State the blood parasite species.
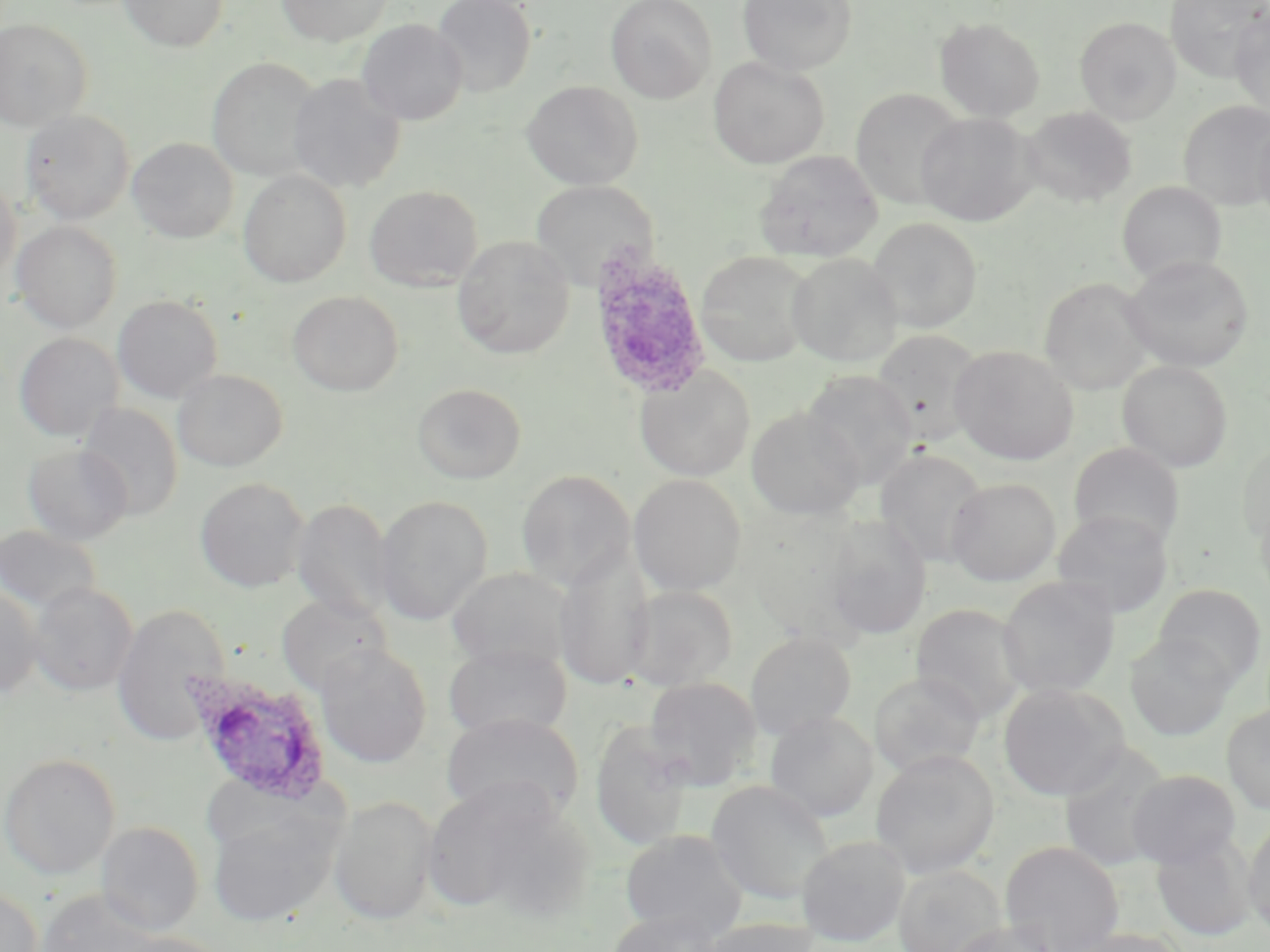
Plasmodium ovale.

Approximate bounding boxes as [x1, y1, x2, y2] in pixels. Plasmodium ovale-infected red blood cell locations: [586, 247, 714, 401], [186, 672, 334, 804]. Uninfected red blood cell locations: [120, 0, 228, 52], [276, 0, 392, 46], [432, 0, 537, 97], [606, 0, 717, 103], [737, 0, 857, 76], [1165, 0, 1269, 83], [1229, 10, 1270, 118], [1075, 16, 1181, 124], [935, 17, 1045, 121], [0, 18, 92, 131], [357, 19, 468, 125], [207, 57, 323, 180], [709, 57, 829, 169], [287, 73, 406, 193], [522, 81, 643, 191], [851, 88, 966, 209], [1179, 101, 1270, 210], [1022, 106, 1138, 207], [20, 110, 135, 224], [917, 112, 1038, 226], [1252, 115, 1270, 230], [128, 138, 238, 242], [755, 150, 883, 262], [238, 170, 351, 287], [0, 179, 20, 282], [531, 181, 657, 289], [1117, 181, 1226, 284], [364, 185, 483, 291], [867, 217, 982, 333], [12, 221, 123, 333], [452, 236, 575, 359], [696, 251, 813, 367], [787, 252, 902, 368], [1122, 254, 1254, 372], [1039, 277, 1156, 395], [287, 290, 403, 396], [112, 294, 223, 403], [872, 330, 985, 446], [14, 332, 123, 442], [950, 345, 1078, 465], [1117, 360, 1233, 472], [634, 366, 755, 482], [173, 368, 287, 471], [801, 370, 917, 491], [412, 382, 527, 484], [78, 403, 184, 521], [746, 407, 864, 521], [1237, 440, 1270, 548], [1068, 442, 1185, 552], [23, 443, 132, 545], [874, 449, 988, 567], [516, 469, 634, 591], [628, 474, 747, 596], [194, 477, 309, 592], [946, 477, 1060, 586], [374, 494, 491, 625], [1254, 496, 1270, 606], [292, 498, 396, 624], [1052, 510, 1174, 617], [823, 516, 932, 639], [0, 524, 102, 614], [553, 547, 654, 692], [446, 567, 573, 672], [997, 575, 1120, 699], [28, 581, 138, 696], [0, 583, 42, 700], [1153, 584, 1266, 689], [625, 585, 738, 691], [275, 594, 391, 695], [111, 603, 231, 747], [910, 603, 1030, 724], [745, 632, 856, 740], [1126, 633, 1235, 740], [315, 643, 432, 768], [443, 643, 572, 741], [869, 672, 985, 778], [643, 676, 762, 790], [998, 683, 1129, 801], [1222, 704, 1270, 814], [440, 712, 584, 823], [764, 712, 878, 823], [590, 724, 696, 850], [1058, 744, 1173, 872], [871, 751, 1000, 878], [1, 753, 120, 880], [1127, 769, 1241, 869], [422, 780, 590, 921], [706, 780, 834, 904], [329, 796, 439, 925], [206, 800, 342, 928], [1242, 818, 1270, 935], [97, 821, 205, 936], [620, 829, 748, 942], [1151, 833, 1255, 941], [796, 835, 910, 946], [1000, 840, 1124, 952], [893, 865, 1005, 952], [0, 884, 43, 952], [34, 889, 166, 952], [605, 911, 722, 952], [699, 918, 817, 952], [947, 920, 1060, 952], [1062, 927, 1190, 952], [109, 932, 234, 952]. May-Grünwald-Giemsa-stained preparation. Thin blood film. Optical microscopy. 1000x magnification. Image is 1270×952 pixels. Single field of view.